Report the malaria status of this cell.
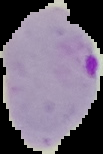
Parasitized.

image_size: 103×154 pixels
image_type: segmented cell region on a black background
preparation: thin blood film